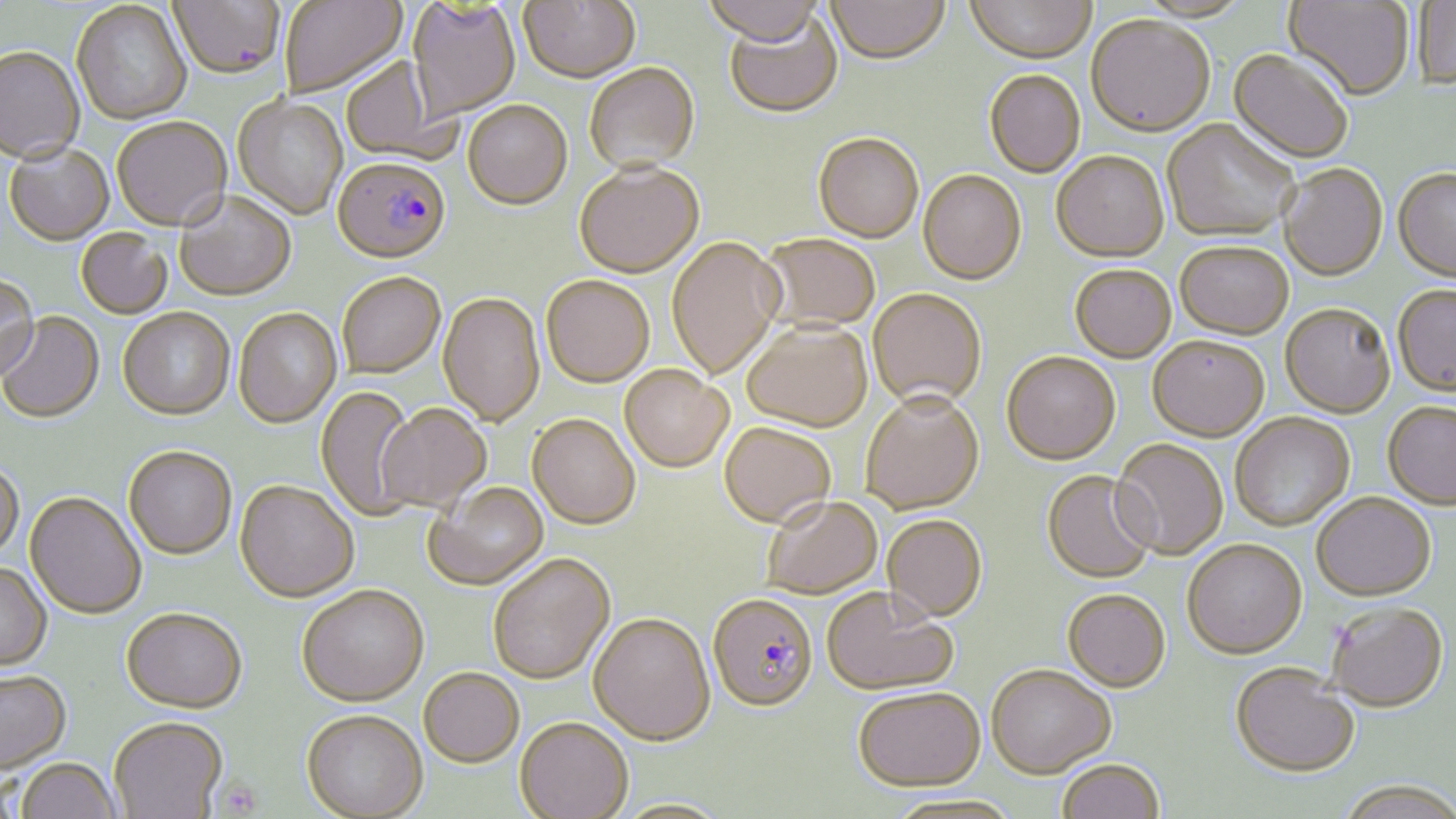
slide-level diagnosis = Plasmodium falciparum
uninfected red blood cell locations = approximate bounding boxes as [x1, y1, x2, y2] in pixels: [167, 0, 285, 79], [279, 0, 407, 98], [518, 0, 640, 86], [701, 0, 822, 50], [825, 0, 950, 68], [965, 0, 1097, 65], [407, 1, 520, 122], [1283, 1, 1414, 104], [1411, 1, 1456, 91], [71, 2, 192, 125], [723, 11, 843, 120], [1086, 18, 1215, 140], [0, 46, 85, 163], [1227, 51, 1353, 165], [340, 58, 447, 163], [585, 65, 701, 176], [984, 71, 1085, 179], [233, 95, 347, 219], [463, 102, 572, 212], [112, 117, 232, 231], [1162, 121, 1298, 244], [813, 135, 924, 245], [4, 143, 115, 245], [1051, 154, 1170, 265], [574, 164, 704, 279], [1279, 166, 1387, 283], [1393, 170, 1456, 286], [918, 172, 1026, 287], [173, 191, 296, 300], [76, 229, 172, 319], [758, 235, 880, 334], [666, 237, 784, 379], [1175, 244, 1294, 341], [1070, 266, 1177, 364], [337, 272, 446, 378], [0, 274, 40, 382], [541, 275, 654, 388], [1392, 288, 1456, 401], [868, 291, 987, 410], [438, 293, 545, 427], [1280, 306, 1395, 419], [118, 307, 235, 419], [233, 308, 342, 428], [0, 312, 104, 424], [741, 322, 872, 432], [1147, 337, 1269, 443], [1000, 352, 1121, 466], [620, 364, 732, 472], [315, 386, 419, 521], [861, 392, 984, 514], [376, 404, 490, 512], [1383, 404, 1455, 510], [527, 413, 640, 529], [1230, 414, 1355, 531], [719, 421, 836, 528], [1111, 440, 1229, 561], [123, 445, 237, 560], [0, 462, 24, 561], [1041, 470, 1158, 584], [235, 480, 359, 602], [423, 481, 548, 590], [24, 492, 146, 619], [1311, 494, 1436, 601], [761, 496, 882, 598], [883, 514, 988, 621], [1182, 540, 1307, 661], [487, 553, 616, 684], [0, 562, 52, 673], [296, 585, 428, 708], [821, 587, 960, 695], [1062, 589, 1170, 693], [1325, 602, 1448, 714], [121, 607, 247, 714], [587, 613, 714, 746], [986, 665, 1116, 778], [1230, 666, 1361, 778], [419, 667, 524, 767], [0, 672, 72, 774], [852, 686, 986, 791], [301, 711, 427, 819], [109, 718, 228, 818], [515, 718, 633, 819], [15, 759, 121, 819], [1056, 761, 1165, 819], [1334, 783, 1456, 819]
modality = light microscopy
image size = 1456×819 pixels
magnification = 1000x
platelet locations = approximate bounding boxes as [x1, y1, x2, y2] in pixels: [214, 778, 263, 817]
stain = May-Grünwald-Giemsa
field of view = single
preparation = thin blood smear
Plasmodium falciparum-infected red blood cell locations = approximate bounding boxes as [x1, y1, x2, y2] in pixels: [332, 158, 451, 264], [708, 593, 818, 712]